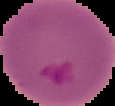
result = Plasmodium parasites identified
image size = 115×106 pixels
preparation = thin blood smear
image type = segmented cell region on a black background